Outline each Plasmodium ovale-infected red blood cell.
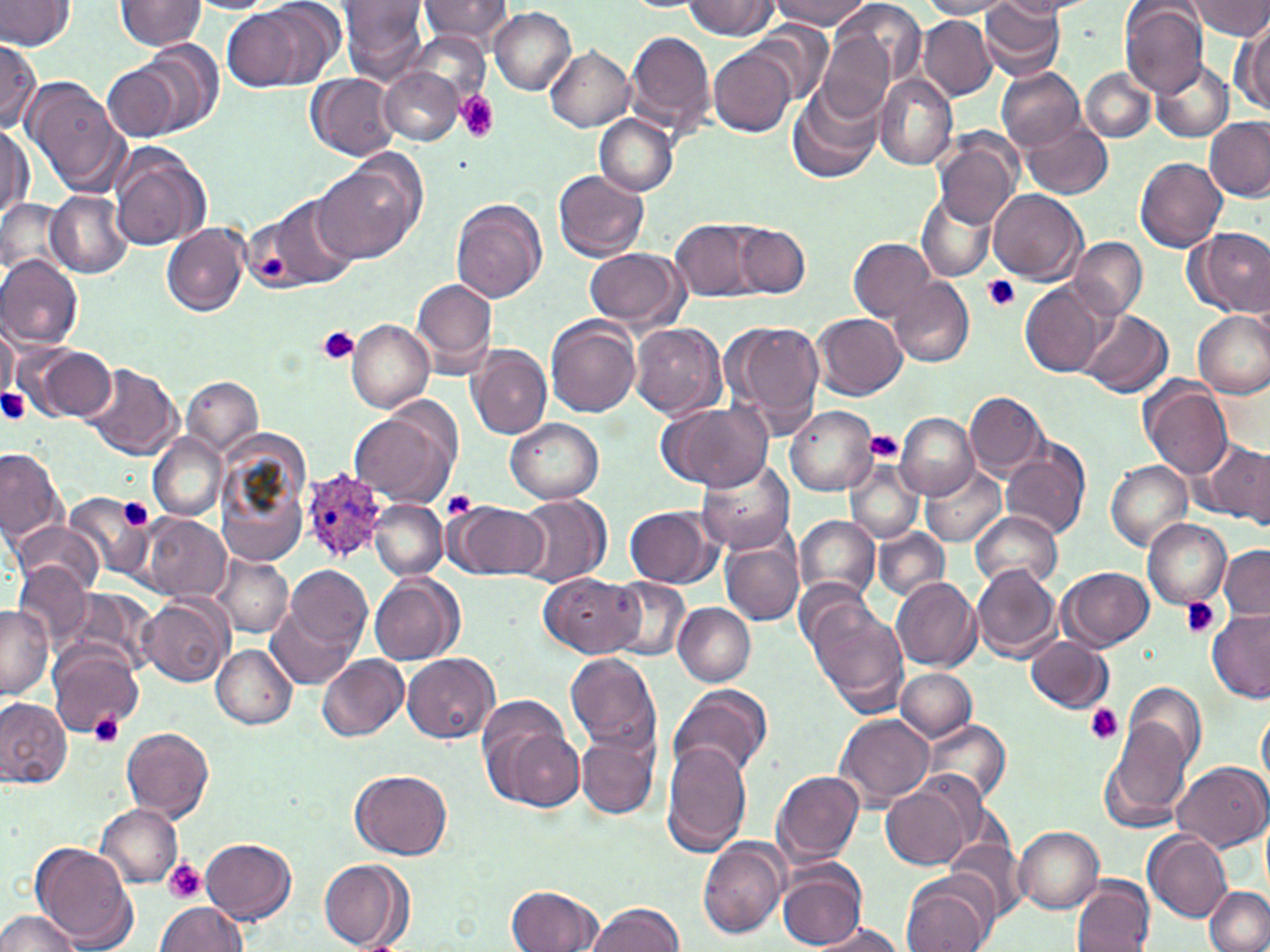
Approximate bounding boxes as (x1,y1)-(x2,y2) corner pairs in pixels.
Plasmodium ovale-infected red blood cells: (300,469)-(388,562).

Platelet locations: (456,91)-(500,143), (983,275)-(1021,312), (318,326)-(358,364), (0,386)-(29,428), (866,432)-(905,462), (443,490)-(477,519), (118,498)-(154,530), (1180,596)-(1221,639), (1085,704)-(1123,744), (89,711)-(125,748), (162,859)-(206,904). Uninfected red blood cell locations: (0,0)-(75,52), (337,0)-(431,84), (417,0)-(513,48), (773,0)-(868,29), (827,0)-(928,93), (995,0)-(1088,18), (1188,0)-(1270,39), (116,1)-(208,51), (185,1)-(277,14), (684,1)-(778,38), (920,1)-(1018,19), (219,2)-(337,93), (977,3)-(1067,81), (1121,3)-(1210,98), (490,8)-(575,95), (919,15)-(997,100), (1234,20)-(1270,117), (745,23)-(834,107), (625,30)-(718,138), (408,31)-(491,106), (816,31)-(897,122), (134,38)-(224,136), (0,39)-(40,134), (545,46)-(636,131), (709,48)-(797,135), (1151,60)-(1233,142), (103,63)-(183,139), (997,67)-(1085,151), (1080,67)-(1157,145), (378,68)-(463,146), (306,73)-(399,162), (22,74)-(128,196), (873,74)-(957,170), (789,85)-(881,185), (593,114)-(680,196), (1202,118)-(1270,202), (1022,119)-(1112,200), (0,125)-(32,219), (930,131)-(1022,230), (108,148)-(210,250), (1135,153)-(1227,252), (313,166)-(417,264), (553,170)-(648,261), (916,187)-(998,282), (989,188)-(1087,284), (47,190)-(132,278), (0,197)-(68,276), (257,198)-(359,292), (452,199)-(548,303), (671,218)-(765,302), (731,222)-(811,299), (162,223)-(249,316), (586,226)-(768,312), (1192,228)-(1269,317), (1069,236)-(1148,320), (848,237)-(936,322), (584,249)-(688,331), (0,256)-(83,349), (413,278)-(499,377), (888,278)-(974,368), (1019,280)-(1112,378), (1193,309)-(1270,399), (1075,310)-(1170,398), (811,313)-(906,400), (546,317)-(642,420), (720,317)-(824,432), (0,320)-(19,404), (347,320)-(435,413), (631,322)-(727,418), (21,345)-(118,423), (468,346)-(551,439), (80,365)-(182,461), (182,376)-(264,460), (1140,381)-(1233,480), (965,390)-(1048,477), (658,401)-(773,490), (348,405)-(458,508), (785,406)-(877,496), (895,412)-(978,499), (506,418)-(604,503), (214,432)-(315,570), (148,435)-(227,522), (1197,441)-(1270,524), (1000,444)-(1090,539), (0,447)-(66,544), (846,457)-(923,544), (696,459)-(796,555), (1105,461)-(1193,551), (921,463)-(1006,547), (63,492)-(154,580), (510,492)-(612,587), (370,500)-(447,579), (445,501)-(548,581), (625,506)-(722,587), (971,512)-(1061,588), (794,514)-(881,606), (138,515)-(229,602), (1142,518)-(1232,608), (11,520)-(104,596), (874,528)-(949,602), (721,537)-(803,627), (1219,544)-(1270,620), (211,553)-(294,638), (14,561)-(94,649), (284,563)-(372,652), (971,564)-(1062,662), (1058,567)-(1154,651), (540,573)-(642,658), (370,576)-(462,665), (890,576)-(981,672), (605,578)-(691,660), (65,590)-(156,673), (138,596)-(233,687), (804,596)-(909,713), (673,603)-(755,686), (268,604)-(356,690), (0,606)-(54,699), (1207,610)-(1270,703), (1026,636)-(1113,714), (47,641)-(143,737), (211,644)-(298,728), (565,652)-(662,756), (403,653)-(500,743), (317,655)-(407,742), (895,668)-(977,742), (1123,681)-(1208,773), (670,684)-(773,784), (0,697)-(72,789), (479,702)-(582,811), (1258,705)-(1270,788), (835,713)-(935,810), (917,718)-(1012,807), (1101,723)-(1192,829), (120,726)-(215,820), (575,732)-(659,821), (661,742)-(753,859), (1172,761)-(1268,851), (352,769)-(452,859), (772,769)-(865,867), (880,781)-(975,872), (96,803)-(183,887), (1012,825)-(1105,913), (945,833)-(1028,923), (1144,833)-(1233,922), (698,837)-(788,940), (200,838)-(297,924), (30,842)-(136,950), (318,859)-(413,951), (776,862)-(867,952), (902,873)-(994,952), (1072,876)-(1155,952), (1204,885)-(1270,952), (507,886)-(604,952), (155,900)-(246,951), (585,902)-(685,952), (0,910)-(83,952), (808,920)-(909,952). Slide-level diagnosis: Plasmodium ovale. One field of a larger specimen. Captured at 1000x magnification. May-Grünwald-Giemsa stain. Thin blood smear. Optical microscopy. Image is 1270×952 pixels.